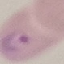
Summary:
  - Result: malaria parasites identified
  - Capture: smartphone camera at the microscope eyepiece
  - Image type: cell patch, automatically extracted from a larger field of view and resized to 64 × 64 pixels
  - Preparation: thin smear
  - Stain: Giemsa